Give the extent of all Plasmodium falciparum-infected red blood cells.
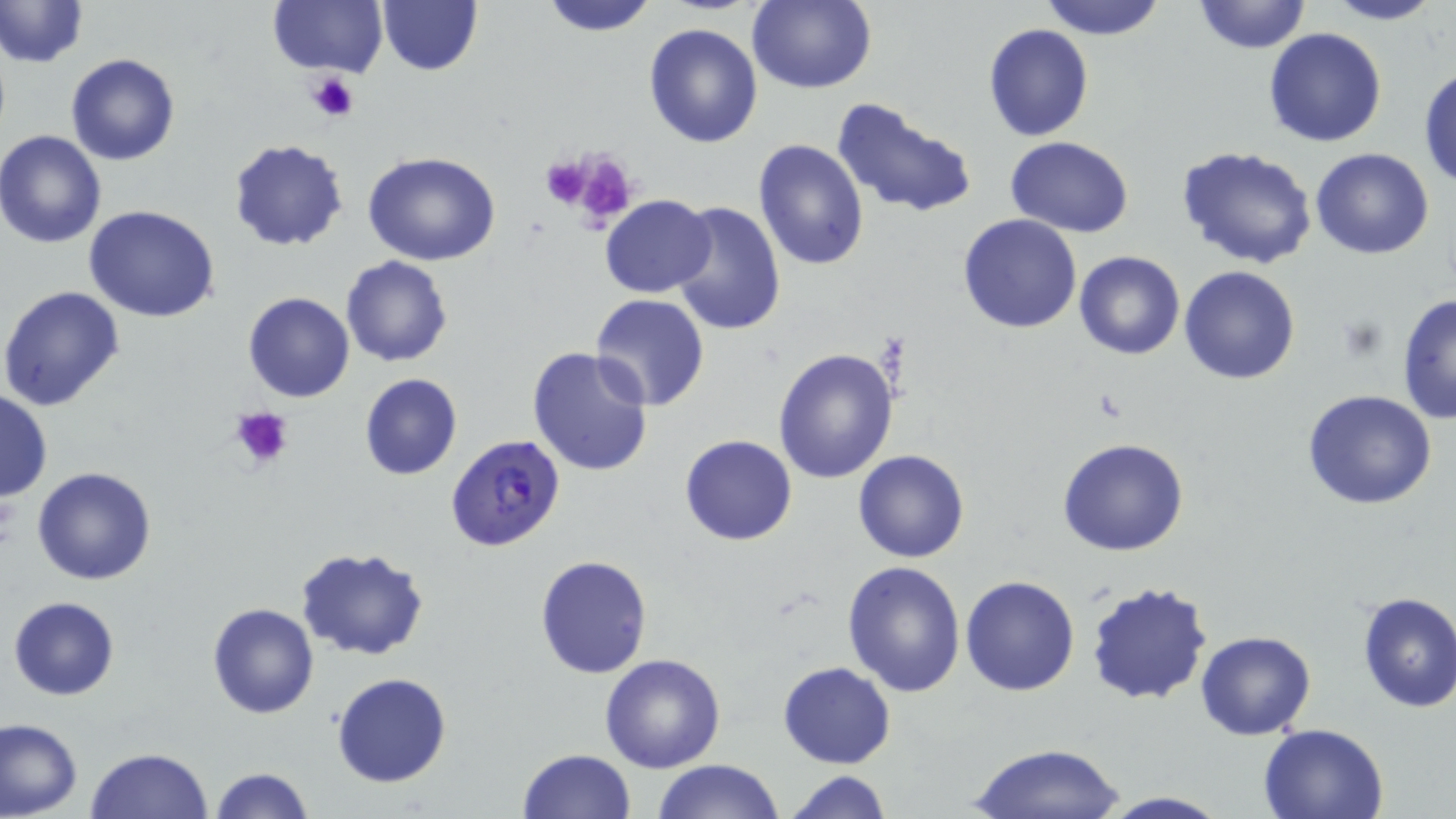
Approximate bounding boxes as named x1/y1/x2/y2 corners in pixels.
Plasmodium falciparum-infected red blood cells: (x1=445, y1=433, x2=566, y2=552).

slide_level_diagnosis: Plasmodium falciparum
uninfected_red_blood_cell_locations: 'approximate bounding boxes as named x1/y1/x2/y2 corners in pixels: (x1=1, y1=0, x2=87, y2=69), (x1=269, y1=0, x2=386, y2=78), (x1=376, y1=0, x2=482, y2=77), (x1=537, y1=0, x2=659, y2=36), (x1=1037, y1=0, x2=1166, y2=41), (x1=1193, y1=0, x2=1311, y2=56), (x1=1317, y1=0, x2=1446, y2=26), (x1=747, y1=1, x2=876, y2=94), (x1=643, y1=23, x2=765, y2=149), (x1=983, y1=23, x2=1094, y2=141), (x1=1263, y1=28, x2=1388, y2=147), (x1=67, y1=53, x2=180, y2=166), (x1=1417, y1=62, x2=1456, y2=190), (x1=34, y1=71, x2=161, y2=210), (x1=831, y1=96, x2=978, y2=221), (x1=0, y1=131, x2=106, y2=248), (x1=1006, y1=136, x2=1133, y2=235), (x1=753, y1=139, x2=869, y2=270), (x1=227, y1=140, x2=349, y2=252), (x1=1178, y1=144, x2=1318, y2=269), (x1=1310, y1=148, x2=1435, y2=259), (x1=362, y1=150, x2=502, y2=266), (x1=599, y1=195, x2=714, y2=298), (x1=668, y1=199, x2=785, y2=337), (x1=83, y1=204, x2=222, y2=323), (x1=957, y1=214, x2=1083, y2=333), (x1=1075, y1=251, x2=1185, y2=360), (x1=341, y1=256, x2=452, y2=368), (x1=1180, y1=266, x2=1301, y2=384), (x1=0, y1=285, x2=124, y2=411), (x1=242, y1=291, x2=355, y2=403), (x1=1396, y1=293, x2=1456, y2=425), (x1=589, y1=294, x2=710, y2=411), (x1=527, y1=347, x2=657, y2=479), (x1=772, y1=347, x2=899, y2=485), (x1=359, y1=373, x2=462, y2=482), (x1=0, y1=389, x2=52, y2=504), (x1=1302, y1=389, x2=1436, y2=511), (x1=679, y1=433, x2=798, y2=545), (x1=1058, y1=437, x2=1190, y2=556), (x1=855, y1=449, x2=970, y2=563), (x1=32, y1=465, x2=159, y2=584), (x1=295, y1=545, x2=433, y2=663), (x1=535, y1=555, x2=652, y2=678), (x1=842, y1=560, x2=966, y2=698), (x1=960, y1=574, x2=1080, y2=695), (x1=1084, y1=578, x2=1214, y2=706), (x1=1355, y1=591, x2=1456, y2=711), (x1=9, y1=596, x2=121, y2=700), (x1=208, y1=602, x2=319, y2=719), (x1=1195, y1=630, x2=1318, y2=742), (x1=599, y1=653, x2=726, y2=773), (x1=776, y1=661, x2=896, y2=768), (x1=332, y1=672, x2=451, y2=787), (x1=0, y1=718, x2=82, y2=817), (x1=1259, y1=722, x2=1389, y2=818), (x1=969, y1=742, x2=1127, y2=819), (x1=85, y1=747, x2=214, y2=819), (x1=516, y1=747, x2=635, y2=818), (x1=652, y1=759, x2=786, y2=819), (x1=209, y1=766, x2=315, y2=819), (x1=783, y1=771, x2=892, y2=818), (x1=1092, y1=791, x2=1232, y2=819)'
image_size: 1456×819 pixels
platelet_locations: 'approximate bounding boxes as named x1/y1/x2/y2 corners in pixels: (x1=309, y1=71, x2=361, y2=122), (x1=557, y1=149, x2=634, y2=221), (x1=538, y1=156, x2=598, y2=210), (x1=228, y1=406, x2=294, y2=471)'
preparation: thin blood smear
stain: May-Grünwald-Giemsa
field_of_view: one of a larger specimen
magnification: 1000x
modality: optical microscopy